Outline each Plasmodium falciparum-infected red blood cell.
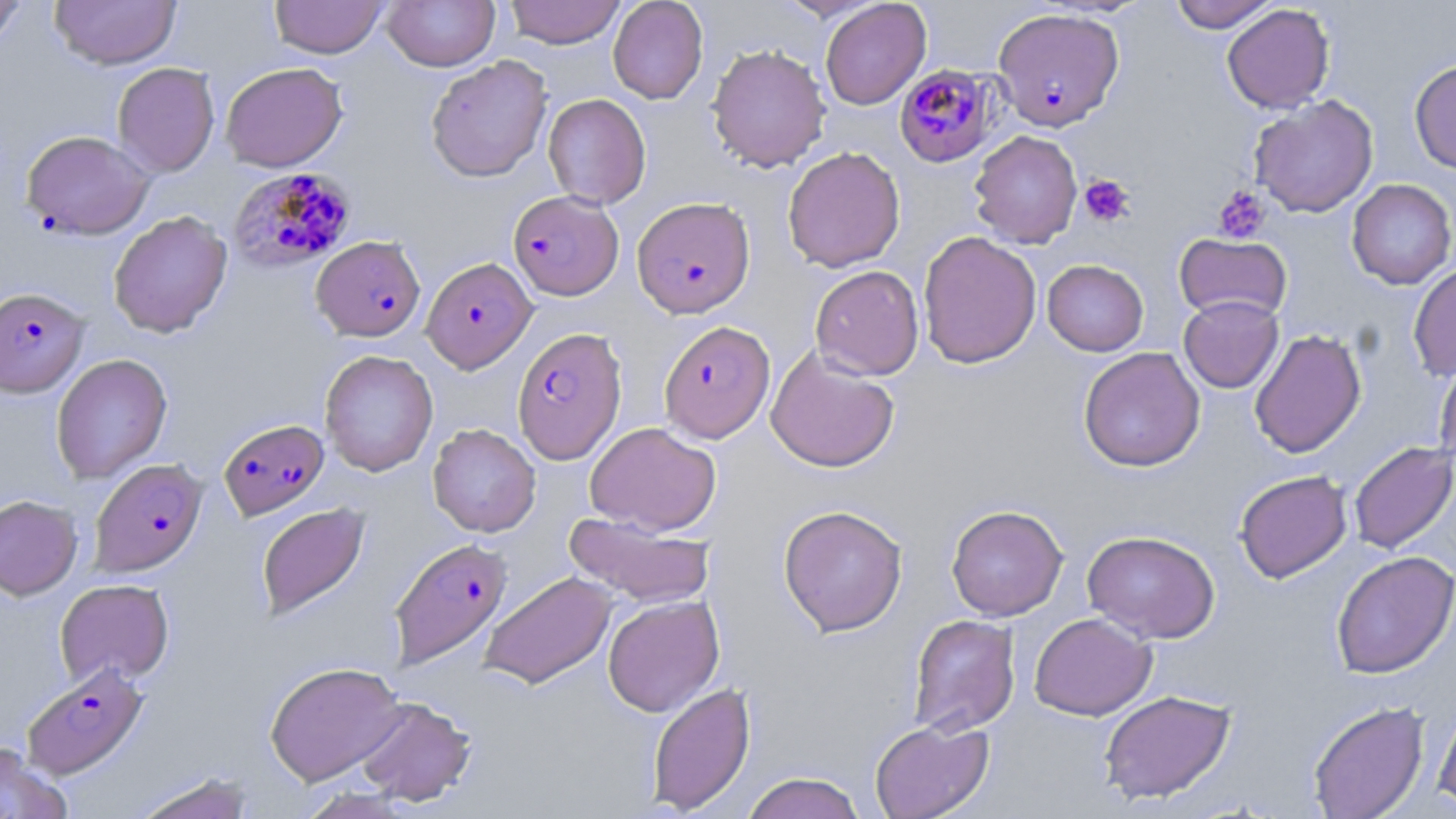
Approximate bounding boxes as named x1/y1/x2/y2 corners in pixels.
Plasmodium falciparum-infected red blood cells: (x1=992, y1=7, x2=1125, y2=132), (x1=893, y1=65, x2=997, y2=167), (x1=20, y1=130, x2=155, y2=240), (x1=229, y1=166, x2=357, y2=271), (x1=507, y1=190, x2=624, y2=301), (x1=632, y1=196, x2=756, y2=318), (x1=311, y1=235, x2=426, y2=341), (x1=421, y1=256, x2=537, y2=373), (x1=1, y1=287, x2=90, y2=398), (x1=659, y1=320, x2=776, y2=443), (x1=512, y1=328, x2=627, y2=463), (x1=218, y1=419, x2=329, y2=520), (x1=89, y1=458, x2=208, y2=577), (x1=389, y1=537, x2=512, y2=669), (x1=22, y1=663, x2=148, y2=779).

{
  "slide_level_diagnosis": "Plasmodium falciparum",
  "field_of_view": "single",
  "platelet_locations": "approximate bounding boxes as named x1/y1/x2/y2 corners in pixels: (x1=1079, y1=174, x2=1135, y2=227), (x1=1213, y1=185, x2=1271, y2=243)",
  "uninfected_red_blood_cell_locations": "approximate bounding boxes as named x1/y1/x2/y2 corners in pixels: (x1=49, y1=0, x2=181, y2=70), (x1=269, y1=0, x2=388, y2=58), (x1=381, y1=0, x2=501, y2=71), (x1=504, y1=0, x2=626, y2=48), (x1=608, y1=0, x2=708, y2=104), (x1=775, y1=0, x2=885, y2=21), (x1=1165, y1=0, x2=1281, y2=32), (x1=0, y1=1, x2=30, y2=51), (x1=820, y1=1, x2=931, y2=110), (x1=1222, y1=3, x2=1335, y2=114), (x1=706, y1=43, x2=831, y2=173), (x1=425, y1=55, x2=552, y2=182), (x1=1409, y1=59, x2=1456, y2=174), (x1=112, y1=62, x2=220, y2=177), (x1=220, y1=62, x2=348, y2=172), (x1=543, y1=93, x2=651, y2=209), (x1=1249, y1=95, x2=1379, y2=218), (x1=968, y1=130, x2=1083, y2=248), (x1=782, y1=146, x2=906, y2=273), (x1=1346, y1=179, x2=1456, y2=289), (x1=108, y1=211, x2=233, y2=338), (x1=917, y1=231, x2=1042, y2=369), (x1=1174, y1=233, x2=1292, y2=323), (x1=1042, y1=259, x2=1148, y2=356), (x1=1408, y1=261, x2=1456, y2=381), (x1=810, y1=265, x2=924, y2=380), (x1=1179, y1=295, x2=1284, y2=393), (x1=1249, y1=329, x2=1366, y2=458), (x1=1078, y1=347, x2=1205, y2=472), (x1=766, y1=348, x2=900, y2=473), (x1=319, y1=349, x2=438, y2=476), (x1=51, y1=353, x2=172, y2=484), (x1=1434, y1=356, x2=1456, y2=472), (x1=585, y1=421, x2=721, y2=535), (x1=427, y1=423, x2=541, y2=537), (x1=1348, y1=441, x2=1456, y2=553), (x1=1234, y1=470, x2=1353, y2=583), (x1=0, y1=495, x2=83, y2=601), (x1=256, y1=502, x2=370, y2=621), (x1=778, y1=504, x2=908, y2=636), (x1=945, y1=504, x2=1068, y2=621), (x1=563, y1=512, x2=714, y2=607), (x1=1082, y1=530, x2=1220, y2=644), (x1=1331, y1=550, x2=1456, y2=679), (x1=480, y1=571, x2=617, y2=689), (x1=54, y1=579, x2=174, y2=686), (x1=603, y1=595, x2=724, y2=717), (x1=1029, y1=613, x2=1157, y2=720), (x1=908, y1=614, x2=1021, y2=737), (x1=264, y1=661, x2=406, y2=786), (x1=646, y1=681, x2=755, y2=814), (x1=1098, y1=689, x2=1236, y2=804), (x1=353, y1=696, x2=477, y2=806), (x1=1433, y1=698, x2=1456, y2=811), (x1=1307, y1=701, x2=1429, y2=819), (x1=869, y1=718, x2=995, y2=819), (x1=0, y1=742, x2=71, y2=819), (x1=130, y1=771, x2=258, y2=819), (x1=741, y1=771, x2=867, y2=819)",
  "magnification": "1000x",
  "image_size": "1456×819 pixels",
  "stain": "May-Grünwald-Giemsa",
  "modality": "optical microscopy",
  "preparation": "thin blood smear"
}